Assess this cell for malaria.
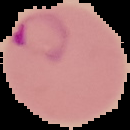

Parasitized.

From a thin blood film. Image is 130×130 pixels. The area outside the segmented cell region is set to black.